Assess for Plasmodium parasites.
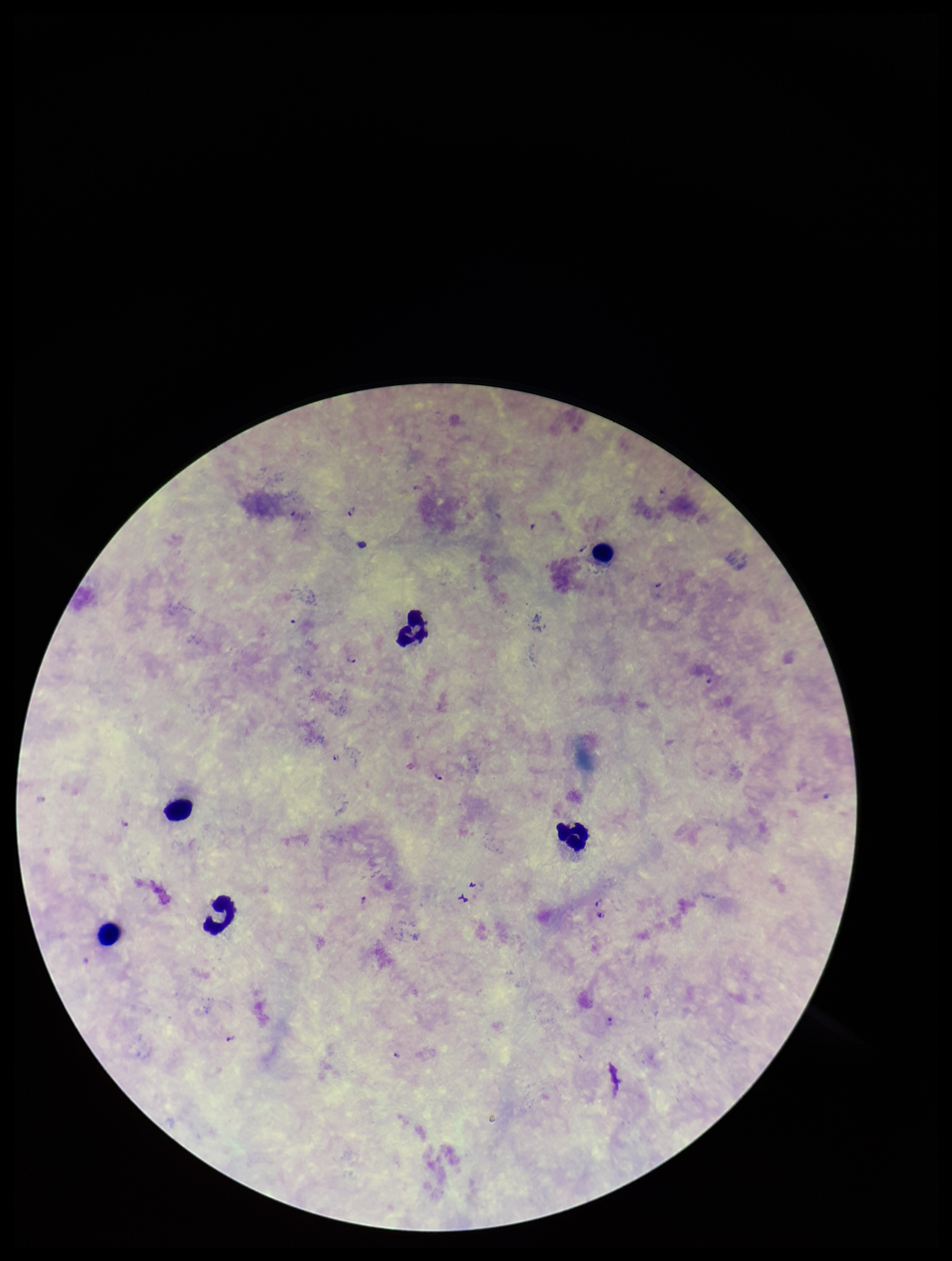

Identified.

Species reported for this patient: Plasmodium falciparum. Photographed through the microscope eyepiece with a smartphone camera. Image is 952×1261 pixels. Parasite count: 9. Preparation: thick. Single field of view. Giemsa stain. Leukocyte count: 6. Patient malaria status: infected.